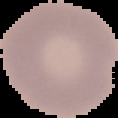
Summary:
  - Image size: 118×118 pixels
  - Malaria status: uninfected
  - Image type: segmented cell region on a black background
  - Preparation: thin blood smear